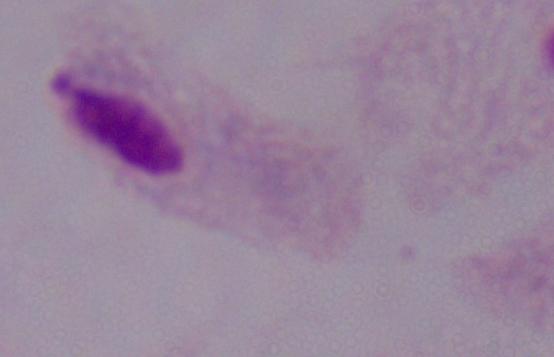

1000x magnification. A trichomonad is seen. Micrograph.